Describe the morphology of the erythrocytes.
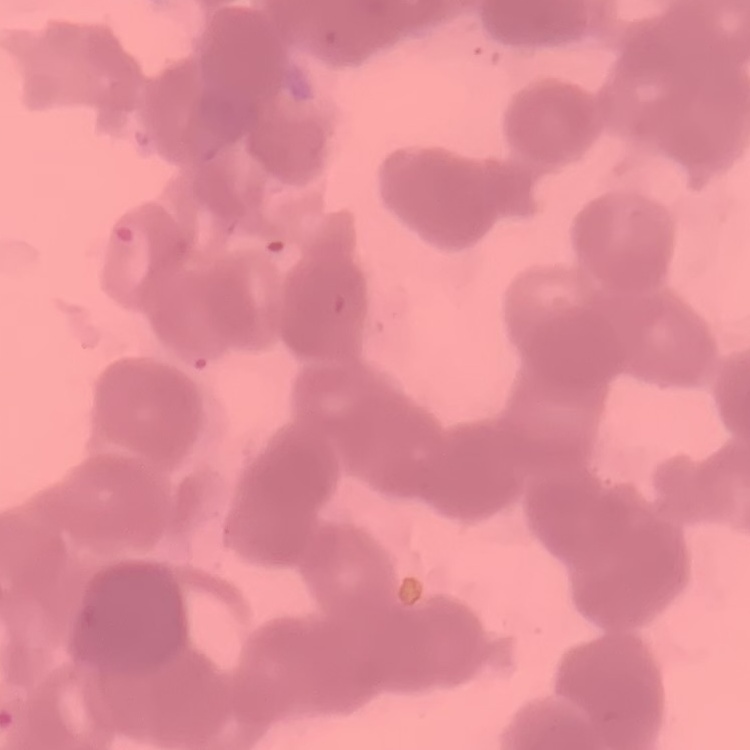
They show rouleaux formation.

Field's or Giemsa stain. Thin peripheral smear. Square crop of a larger photomicrograph.